State which parasite is depicted.
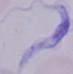
This is a trypanosome.

magnification = 1000x
modality = micrograph